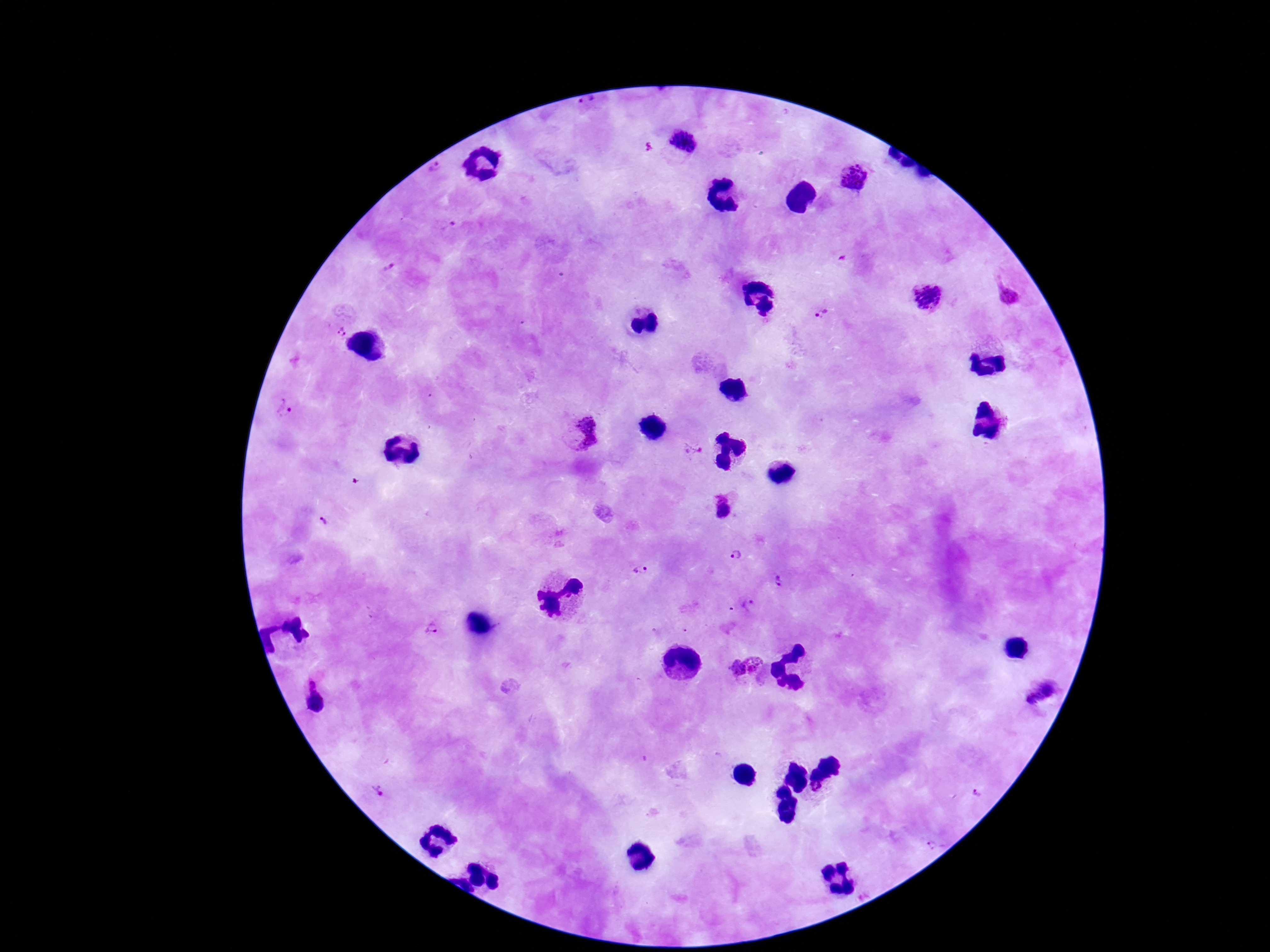

capture: smartphone camera through the microscope eyepiece
plasmodium_parasite_locations: 'approximate centers as (x, y) in pixels: (588, 106), (438, 174), (850, 178), (449, 226), (388, 268), (1007, 291), (926, 293), (820, 314), (337, 329), (286, 411), (578, 432), (693, 450), (723, 507), (736, 555), (640, 568), (777, 581), (748, 603), (432, 629), (745, 671), (1041, 696), (313, 698), (379, 790), (818, 790), (975, 793), (933, 846)'
magnification: 100x
image_size: 1270×952 pixels
field_of_view: one from this slide
stain: Giemsa
patient_malaria_status: positive
preparation: thick blood smear